State which cell type is depicted.
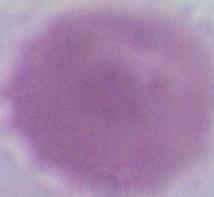
An erythrocyte.

modality = photomicrograph
magnification = 1000x